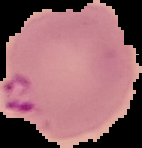
From a thin blood smear. Image is 142×148 pixels. Cell region segmented out of the field of view; the surrounding area is masked to black. Malaria status: parasitized.